Identify the blood parasite species.
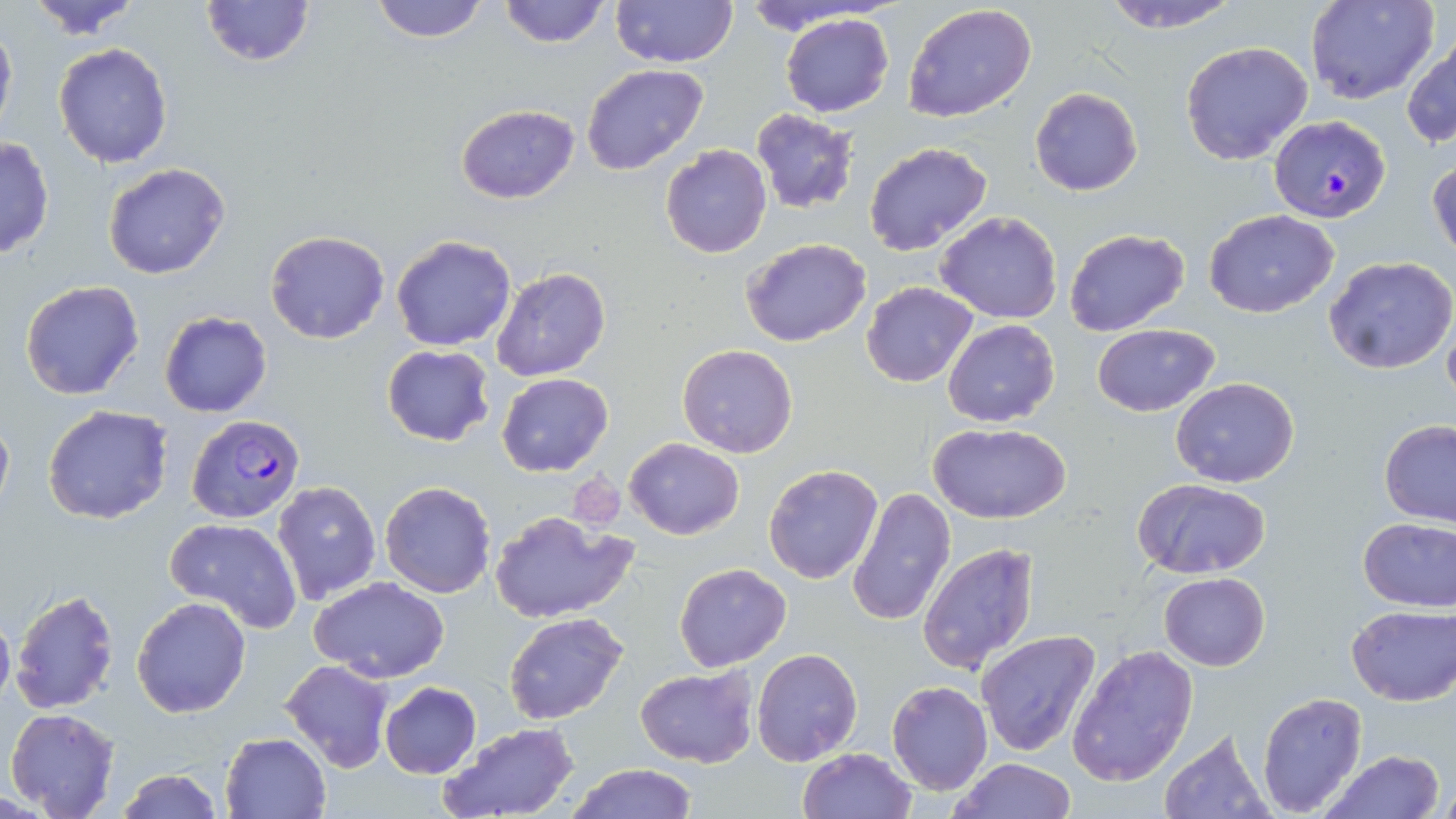

Plasmodium falciparum.

Summary:
  - Coordinate format: approximate bounding boxes as (x1, y1, x2, y2) in pixels
  - Uninfected red blood cell locations: (22, 0, 146, 39), (200, 0, 314, 67), (367, 0, 493, 43), (496, 0, 611, 50), (610, 0, 740, 69), (1095, 0, 1244, 33), (1307, 0, 1439, 103), (903, 4, 1038, 123), (780, 12, 893, 117), (0, 17, 17, 141), (1404, 31, 1455, 150), (53, 41, 174, 169), (1179, 41, 1314, 166), (582, 64, 709, 176), (1030, 88, 1144, 196), (456, 104, 579, 203), (752, 108, 860, 215), (0, 137, 54, 261), (864, 141, 993, 256), (660, 145, 771, 259), (1428, 158, 1455, 265), (103, 163, 231, 279), (935, 210, 1063, 324), (1203, 210, 1339, 316), (1063, 228, 1190, 336), (265, 230, 390, 344), (392, 235, 515, 351), (742, 238, 872, 348), (1325, 256, 1456, 373), (492, 268, 612, 382), (21, 281, 144, 401), (861, 282, 977, 386), (1442, 310, 1456, 408), (158, 312, 272, 418), (942, 319, 1060, 427), (1092, 323, 1219, 415), (678, 344, 798, 457), (381, 345, 495, 447), (496, 373, 613, 476), (1171, 377, 1299, 487), (43, 404, 173, 525), (0, 408, 13, 522), (1378, 419, 1456, 526), (930, 424, 1072, 525), (624, 438, 745, 539), (763, 464, 883, 584), (1132, 477, 1275, 581), (272, 479, 382, 605), (380, 481, 496, 598), (847, 487, 955, 628), (489, 509, 634, 622), (1357, 516, 1456, 612), (165, 517, 302, 631), (918, 542, 1039, 676), (674, 563, 791, 674), (1159, 572, 1270, 672), (310, 575, 450, 682), (10, 589, 119, 714), (132, 597, 250, 717), (1346, 605, 1454, 706), (0, 607, 15, 713), (503, 612, 630, 724), (976, 630, 1102, 757), (1066, 644, 1199, 787), (750, 647, 863, 766), (280, 659, 394, 772), (635, 666, 758, 767), (886, 681, 993, 795), (378, 682, 481, 778), (1256, 692, 1368, 816), (4, 707, 121, 819), (439, 722, 580, 819), (1158, 727, 1274, 818), (220, 731, 330, 817), (797, 748, 916, 819), (1321, 751, 1444, 819), (947, 758, 1078, 818), (563, 762, 696, 819), (113, 769, 224, 818)
  - Plasmodium falciparum-infected red blood cell locations: (1269, 115, 1391, 222), (188, 414, 305, 523)
  - Platelet locations: (570, 472, 626, 530)
  - Stain: May-Grünwald-Giemsa
  - Magnification: 1000x
  - Preparation: thin blood smear
  - Field of view: single
  - Modality: light microscopy
  - Image size: 1456×819 pixels